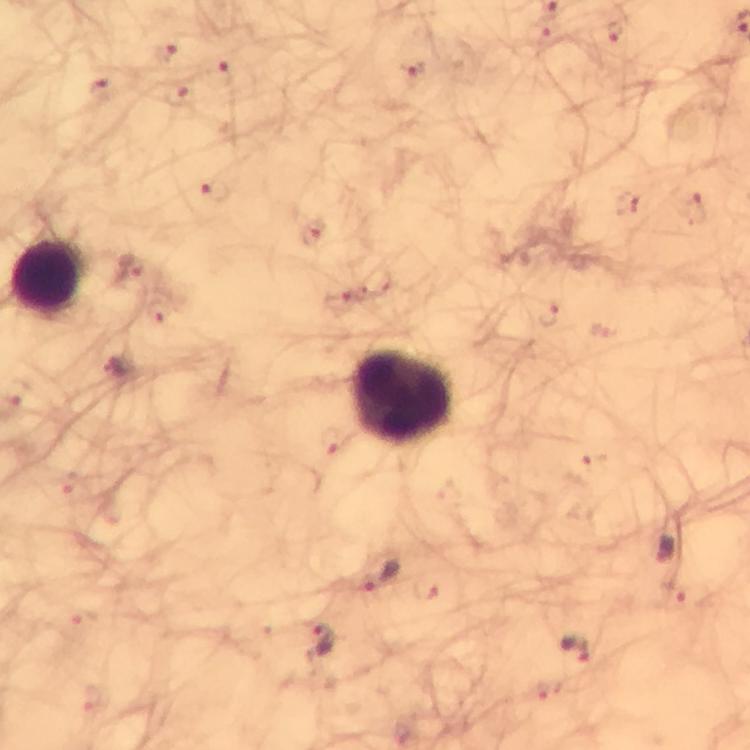
Approximate centers as [x, y] in pixels. Plasmodium parasite locations: [665, 547], [382, 577], [321, 643], [575, 651]. Leukocyte locations: [51, 278], [404, 400]. Smartphone photograph taken through a microscope. 100x magnification. Giemsa-stained preparation. Image is 750×750 pixels. From a diagnostic examination for malaria. A crop from one field of view. Immersion oil applied. Thick blood smear.